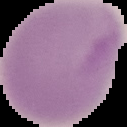
preparation = thin blood smear
malaria status = uninfected
image size = 127×127 pixels
image type = cell region segmented out of the field of view; surrounding area masked to black